Comment on the morphology of the red blood cells.
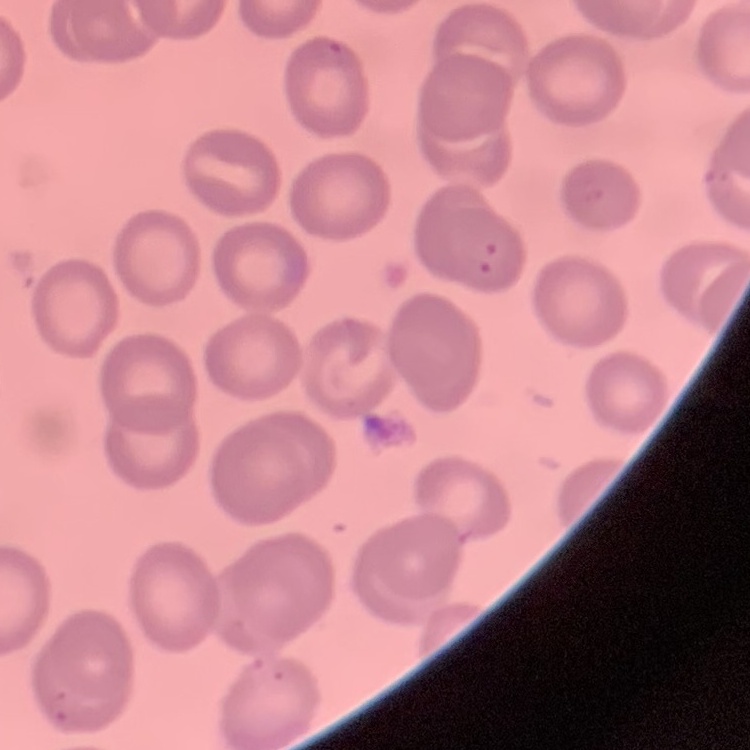
They show no rouleaux formation.

Square crop of a larger photomicrograph. Field's or Giemsa stain. Thin peripheral smear.